Assess this cell for malaria.
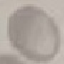

It is uninfected.

Giemsa stain. Cell patch, automatically extracted from a larger field of view and resized to 64 × 64 pixels. Thin blood film. Acquired by smartphone through the microscope eyepiece.